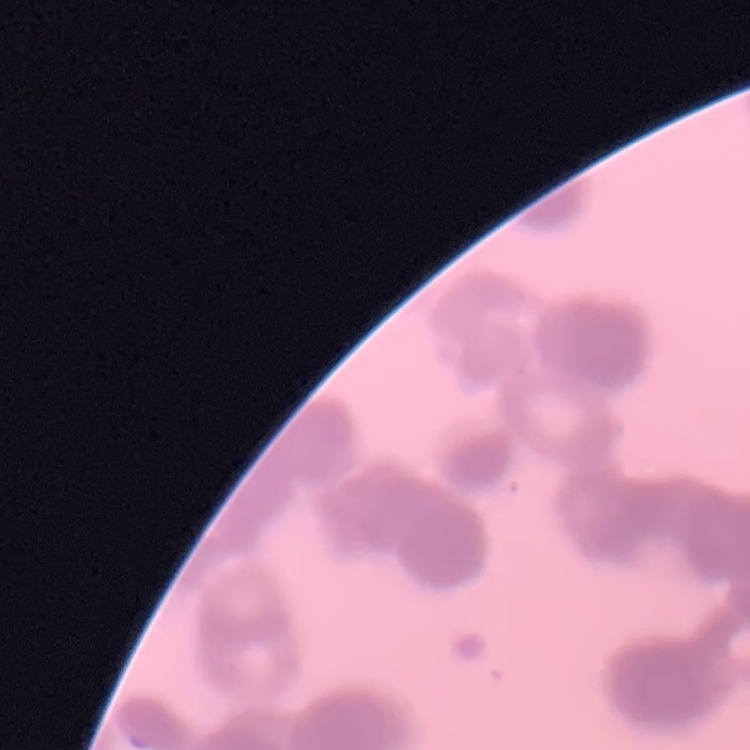

{
  "red_blood_cell_morphology": "rouleaux formation",
  "preparation": "thin blood film",
  "stain": "Field's or Giemsa",
  "image_type": "one tile cut from a larger photomicrograph"
}